Assess this cell for malaria.
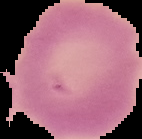

Uninfected.

Summary:
  - Image type: segmented cell region with the area outside set to black
  - Preparation: thin blood film
  - Image size: 142×139 pixels